Assess for malaria.
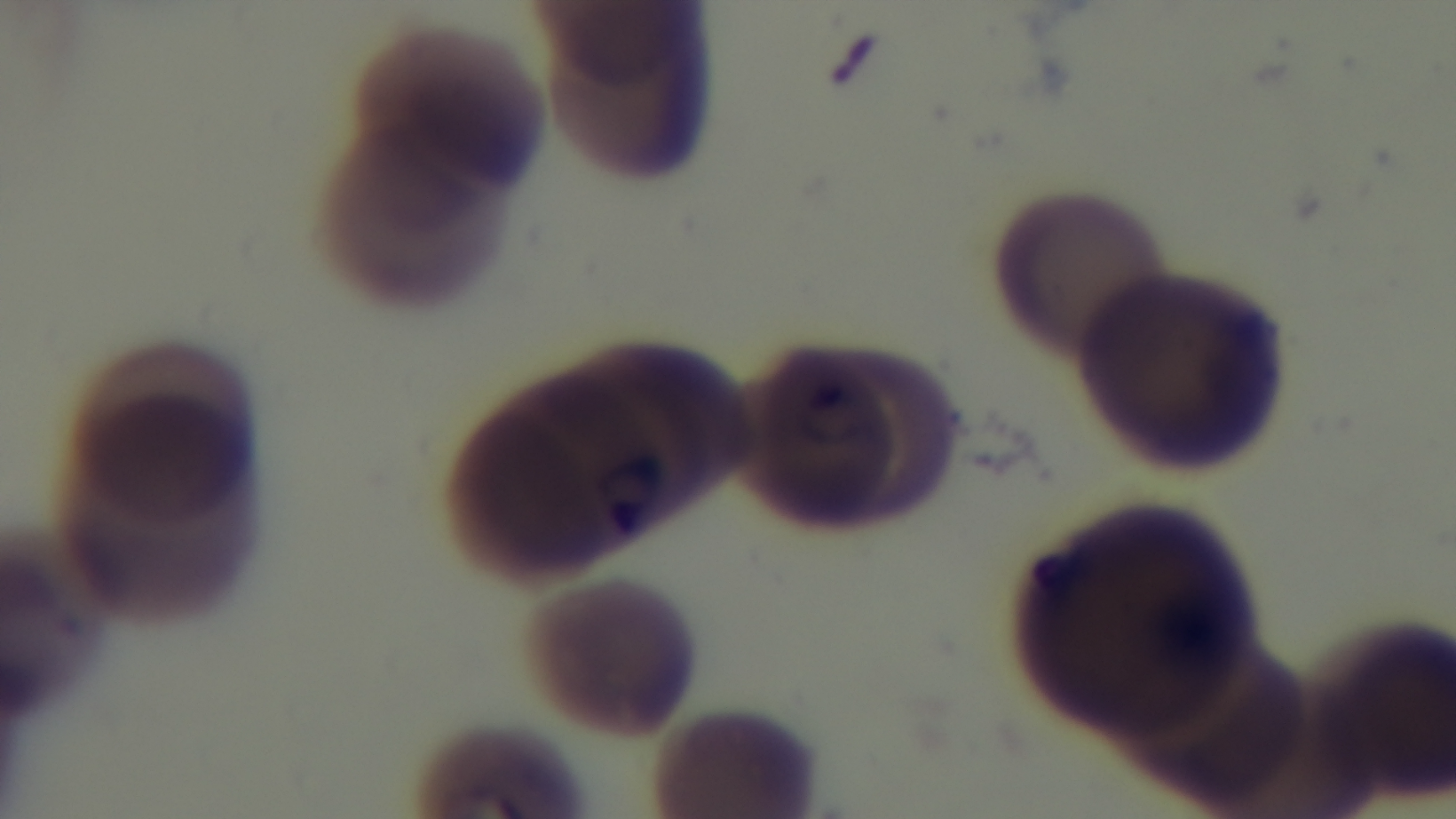
It is infected.

preparation = thin
capture = mounted 4K digital camera
field of view = one from the slide
stain = Giemsa
objective = 100x oil immersion
modality = light microscopy